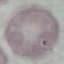

Malaria status: uninfected. Giemsa stain. Acquired by smartphone through the microscope eyepiece. Cell patch, automatically extracted from a larger field of view and resized to 64 × 64 pixels. Thin blood smear.